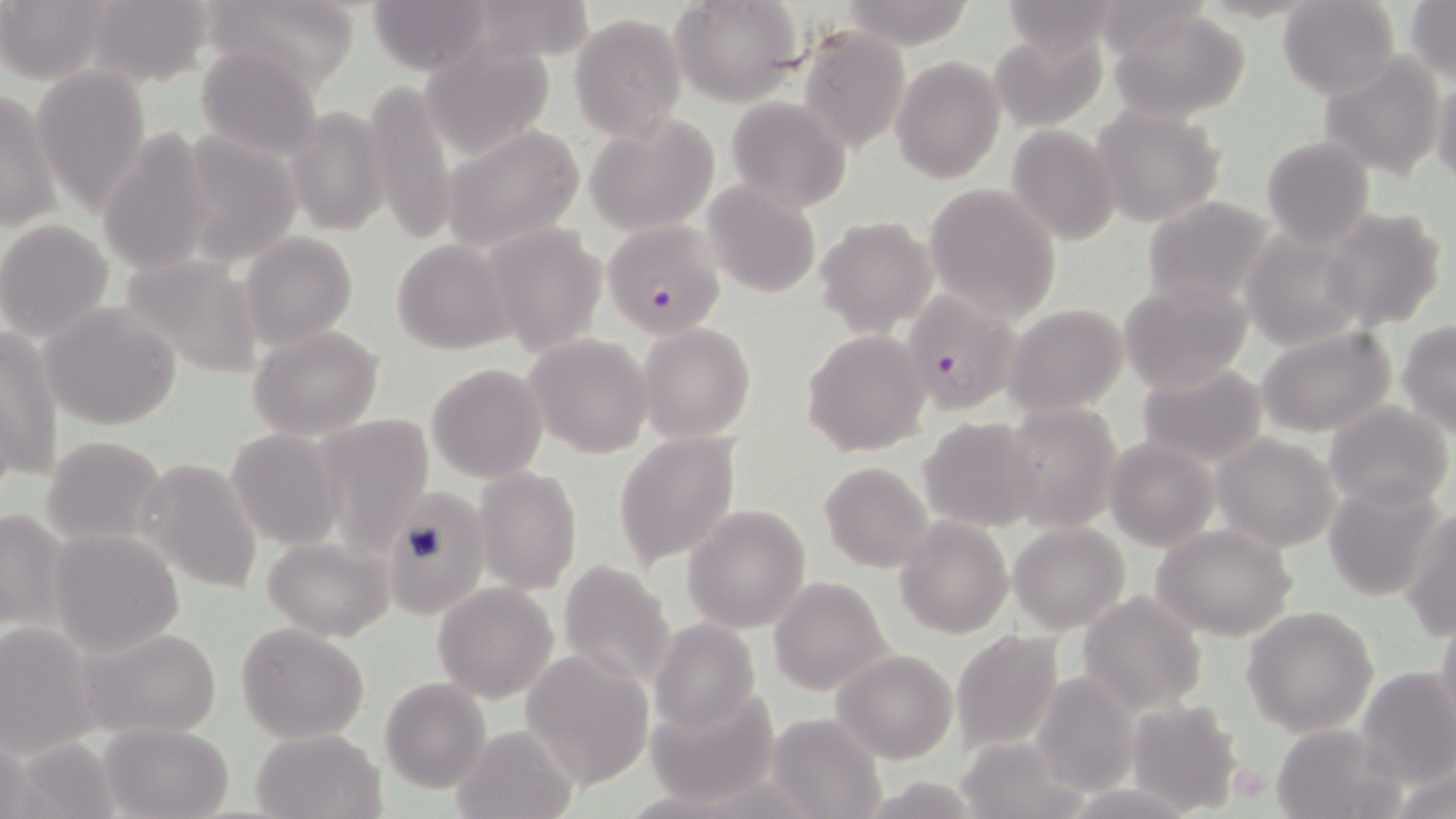
Summary:
  - Coordinate format: approximate bounding boxes as (x1, y1, x2, y2) in pixels
  - Uninfected red blood cell locations: (81, 0, 219, 90), (201, 0, 364, 92), (365, 0, 498, 76), (458, 0, 596, 69), (672, 0, 804, 106), (1277, 0, 1400, 99), (1406, 0, 1455, 84), (836, 1, 977, 48), (995, 1, 1129, 60), (1, 2, 112, 85), (1105, 8, 1251, 122), (570, 13, 686, 139), (798, 27, 911, 152), (992, 28, 1107, 133), (417, 39, 557, 160), (193, 42, 326, 161), (1315, 53, 1445, 179), (890, 56, 1007, 183), (33, 65, 151, 210), (1431, 74, 1456, 189), (362, 80, 456, 246), (0, 91, 61, 236), (726, 97, 852, 213), (285, 104, 391, 236), (1090, 105, 1224, 227), (584, 116, 719, 236), (440, 124, 585, 253), (1007, 125, 1122, 245), (174, 129, 302, 266), (99, 130, 219, 275), (1261, 135, 1377, 247), (701, 182, 821, 297), (922, 182, 1061, 321), (1140, 195, 1279, 309), (1318, 208, 1450, 334), (815, 216, 939, 339), (0, 220, 114, 342), (483, 222, 609, 358), (1239, 225, 1371, 349), (241, 232, 357, 350), (390, 239, 514, 354), (119, 253, 263, 379), (1119, 280, 1252, 394), (39, 302, 184, 430), (1005, 304, 1128, 416), (1398, 322, 1456, 437), (639, 323, 756, 443), (249, 324, 384, 440), (1, 326, 63, 485), (1258, 326, 1397, 438), (802, 329, 933, 458), (523, 334, 655, 458), (425, 363, 548, 483), (1136, 363, 1271, 469), (1002, 400, 1123, 536), (1324, 400, 1455, 513), (308, 413, 435, 547), (919, 417, 1042, 532), (226, 428, 345, 549), (613, 431, 742, 567), (1214, 434, 1342, 552), (43, 435, 164, 545), (1103, 436, 1219, 552), (135, 458, 263, 594), (818, 461, 936, 572), (472, 466, 583, 595), (1322, 481, 1447, 600), (381, 491, 488, 613), (683, 503, 812, 632), (1, 506, 68, 634), (1403, 509, 1455, 639), (895, 517, 1013, 639), (1008, 522, 1130, 633), (1153, 525, 1298, 641), (48, 528, 187, 657), (263, 537, 395, 640), (559, 557, 677, 691), (769, 576, 893, 696), (431, 582, 558, 704), (1077, 591, 1207, 715), (1243, 606, 1380, 736), (1434, 609, 1456, 736), (649, 618, 759, 736), (0, 623, 98, 755), (74, 623, 223, 742), (235, 623, 370, 745), (950, 630, 1066, 755), (520, 648, 655, 789), (831, 648, 958, 764), (1355, 666, 1455, 787), (1032, 675, 1138, 793), (378, 677, 492, 795), (649, 693, 777, 808), (1126, 699, 1243, 813), (767, 714, 884, 818), (99, 722, 235, 819), (1268, 722, 1400, 819), (451, 723, 581, 819), (251, 728, 385, 819), (956, 736, 1088, 819), (5, 737, 120, 819), (1389, 762, 1456, 819), (858, 776, 990, 816)
  - Plasmodium falciparum-infected red blood cell locations: (601, 218, 725, 339), (900, 291, 1023, 416)
  - Platelet locations: (1229, 763, 1270, 803)
  - Slide-level diagnosis: Plasmodium falciparum
  - Stain: May-Grünwald-Giemsa
  - Field of view: single
  - Modality: light microscopy
  - Preparation: thin blood film
  - Image size: 1456×819 pixels
  - Magnification: 1000x